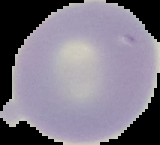 Image is 160×145 pixels. From a thin blood film. The area outside the segmented cell region is set to black. Result: no Plasmodium parasites detected.